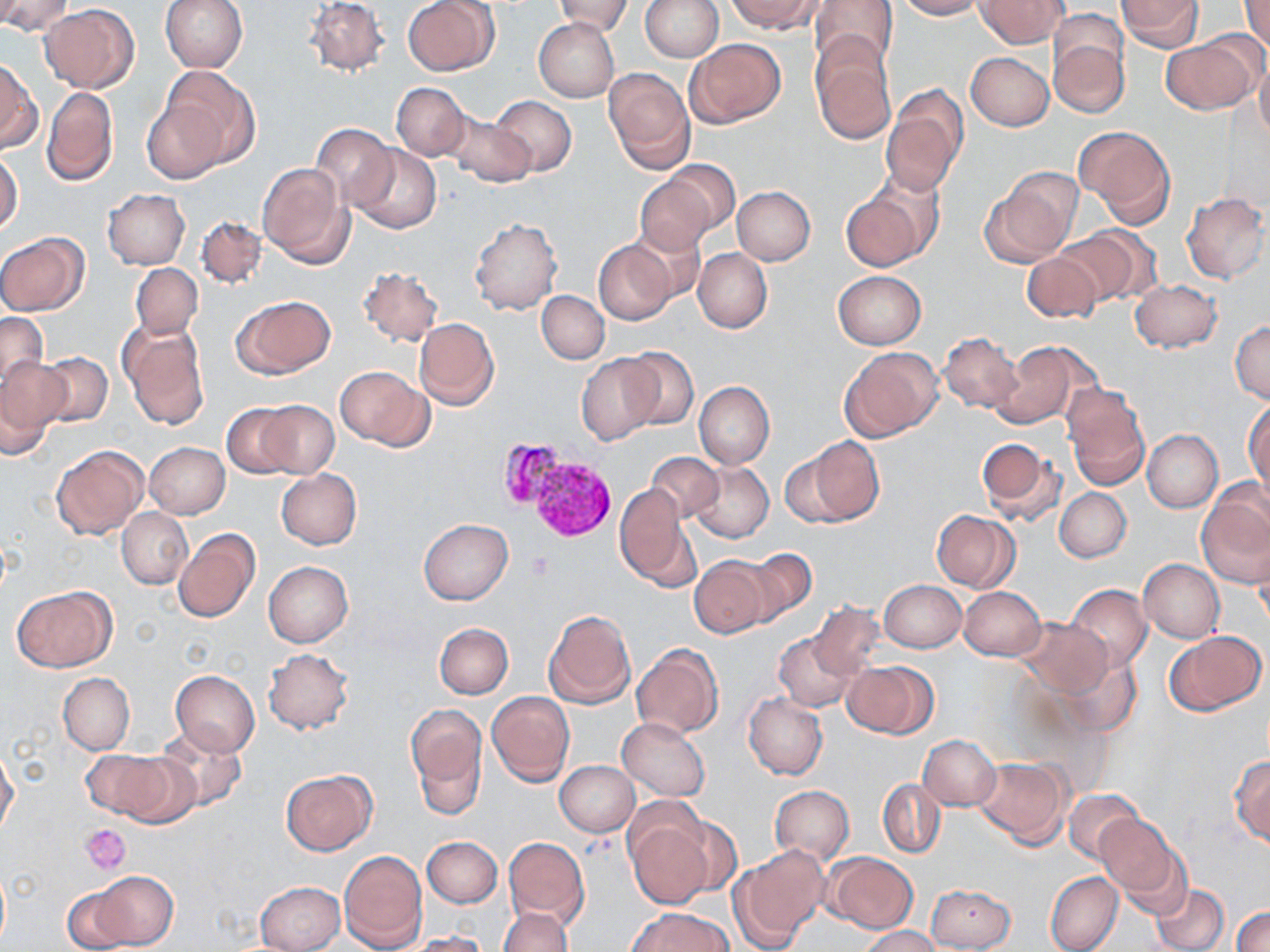 Approximate bounding boxes as [x1, y1, x2, y2] in pixels. Platelet locations: [529, 552, 555, 577], [81, 824, 131, 875]. Plasmodium vivax-infected red blood cell locations: [493, 436, 564, 508], [530, 460, 620, 541]. Uninfected red blood cell locations: [0, 0, 74, 37], [159, 0, 247, 72], [305, 0, 389, 76], [403, 0, 498, 75], [554, 0, 632, 36], [642, 0, 723, 62], [728, 0, 821, 34], [809, 0, 898, 74], [896, 0, 983, 20], [975, 0, 1068, 48], [1116, 0, 1203, 51], [1239, 0, 1270, 50], [40, 4, 140, 93], [644, 6, 757, 89], [533, 17, 619, 102], [1049, 30, 1129, 120], [1161, 36, 1259, 114], [686, 38, 786, 127], [810, 41, 897, 144], [966, 52, 1054, 131], [1255, 56, 1270, 145], [0, 60, 41, 154], [161, 67, 255, 172], [604, 67, 695, 172], [392, 82, 470, 160], [42, 85, 118, 187], [882, 90, 967, 195], [489, 95, 577, 177], [142, 97, 228, 183], [444, 112, 537, 189], [312, 123, 397, 209], [1076, 124, 1175, 227], [350, 143, 441, 234], [0, 152, 22, 233], [659, 159, 740, 236], [258, 161, 354, 268], [982, 171, 1080, 266], [634, 174, 716, 256], [732, 186, 815, 265], [841, 187, 931, 272], [103, 188, 190, 269], [1182, 192, 1269, 284], [196, 216, 267, 290], [469, 218, 562, 315], [627, 221, 707, 302], [1053, 228, 1150, 308], [0, 232, 88, 316], [593, 239, 677, 326], [693, 248, 771, 333], [1022, 251, 1103, 323], [131, 262, 202, 339], [357, 265, 444, 347], [832, 271, 927, 349], [1131, 280, 1223, 353], [537, 290, 609, 364], [231, 296, 336, 379], [0, 311, 48, 391], [414, 318, 499, 410], [1231, 320, 1270, 404], [120, 322, 208, 430], [939, 332, 1023, 414], [989, 341, 1083, 430], [620, 346, 698, 429], [839, 346, 943, 442], [36, 352, 114, 427], [577, 354, 664, 444], [0, 355, 71, 447], [335, 367, 433, 451], [694, 381, 774, 468], [1061, 385, 1149, 489], [1245, 398, 1270, 495], [253, 401, 340, 478], [222, 403, 300, 479], [1142, 429, 1223, 511], [804, 436, 883, 524], [976, 436, 1066, 526], [144, 442, 230, 519], [51, 445, 148, 539], [779, 451, 859, 527], [648, 453, 723, 524], [689, 463, 773, 543], [276, 469, 361, 550], [615, 483, 694, 589], [1198, 487, 1270, 591], [1054, 488, 1131, 563], [117, 508, 192, 589], [931, 510, 1019, 592], [418, 519, 512, 605], [173, 529, 260, 622], [1250, 541, 1270, 632], [740, 548, 818, 625], [689, 556, 771, 638], [1138, 558, 1224, 642], [263, 561, 353, 647], [880, 579, 965, 652], [1064, 584, 1152, 674], [13, 586, 114, 672], [961, 587, 1046, 661], [808, 601, 882, 680], [543, 609, 637, 710], [1015, 618, 1112, 699], [433, 623, 513, 698], [1163, 630, 1266, 716], [774, 631, 858, 711], [630, 644, 721, 738], [263, 648, 353, 735], [1046, 649, 1143, 739], [843, 660, 938, 739], [170, 669, 260, 756], [58, 673, 134, 755], [486, 691, 575, 787], [743, 692, 827, 780], [407, 705, 485, 808], [616, 717, 710, 801], [152, 726, 248, 811], [919, 734, 999, 810], [0, 748, 19, 836], [84, 748, 187, 824], [1229, 755, 1270, 846], [972, 756, 1069, 846], [556, 760, 639, 836], [280, 770, 376, 855], [878, 778, 946, 858], [770, 785, 853, 864], [1064, 789, 1144, 864], [1095, 814, 1181, 899], [626, 817, 715, 910], [423, 836, 502, 908], [503, 837, 589, 929], [734, 847, 829, 946], [339, 849, 428, 952], [824, 851, 917, 933], [86, 871, 178, 949], [1045, 871, 1123, 952], [62, 881, 145, 952], [254, 881, 343, 952], [1151, 881, 1229, 952], [927, 882, 1016, 952], [1233, 906, 1270, 952], [629, 907, 731, 952], [499, 908, 572, 952], [860, 926, 942, 951], [406, 931, 490, 952]. Slide-level diagnosis: Plasmodium vivax. May-Grünwald-Giemsa-stained preparation. Image is 1270×952 pixels. One field of a larger specimen. Light microscopy. Thin blood smear. 1000x magnification.